Classify this cell by malaria status.
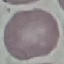

Uninfected.

Automatically extracted cell patch, resized to 64 × 64 pixels. Giemsa stain. Thin blood film. Acquired by smartphone through the microscope eyepiece.